Assess for malaria.
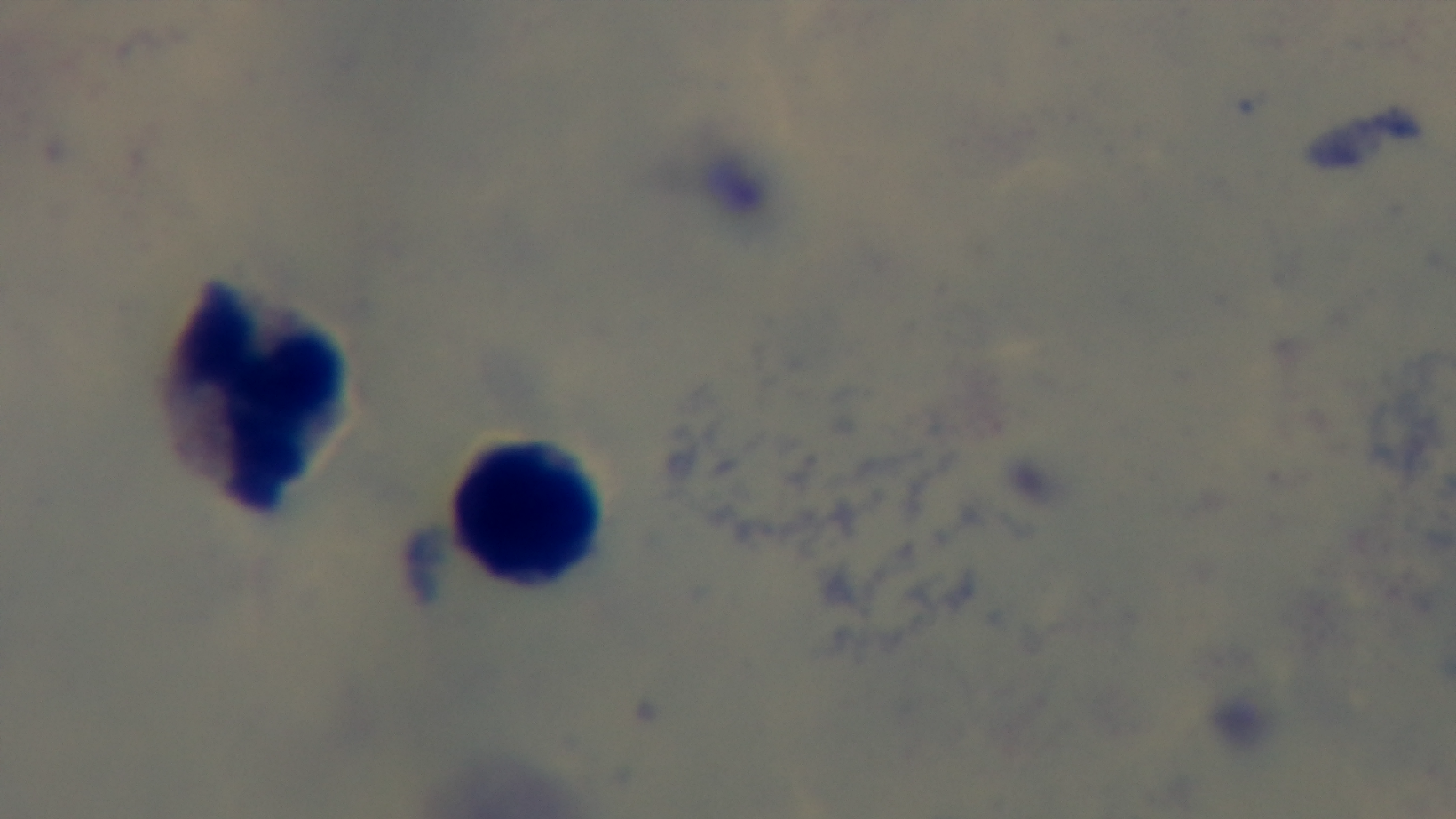
Negative.

field of view = one from the slide
capture = mounted 4K digital camera
modality = light microscopy
preparation = thick
stain = Giemsa
objective = 100x oil immersion